Comment on the morphology of the erythrocytes.
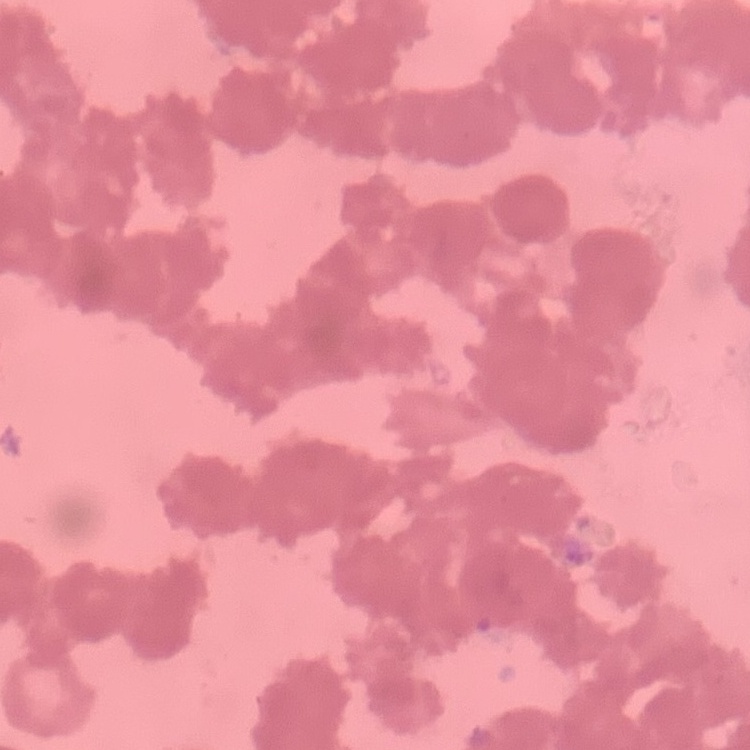

They show rouleaux formation.

preparation = thin blood smear
stain = Field's or Giemsa
image type = square crop of a larger photomicrograph